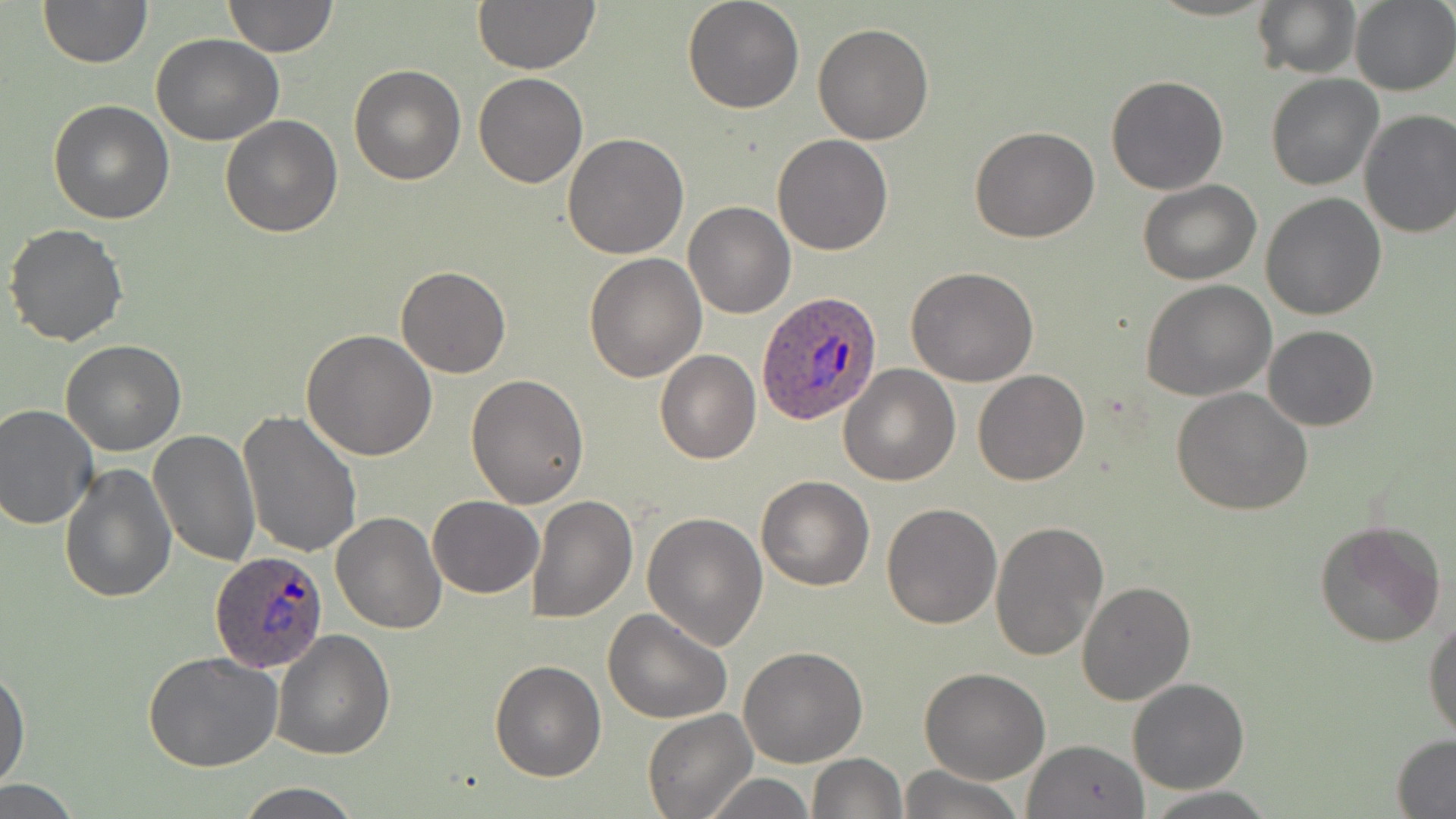 Approximate bounding boxes as (x1, y1, x2, y2) in pixels. Uninfected red blood cell locations: (38, 0, 151, 67), (222, 0, 339, 57), (471, 0, 602, 75), (682, 0, 804, 114), (1251, 0, 1360, 80), (1349, 1, 1456, 94), (812, 22, 936, 145), (151, 33, 283, 146), (349, 63, 466, 185), (473, 73, 588, 188), (1106, 74, 1229, 195), (1265, 74, 1383, 190), (48, 99, 176, 223), (1357, 109, 1456, 239), (221, 116, 343, 238), (970, 127, 1098, 244), (563, 134, 689, 259), (771, 134, 894, 257), (1137, 179, 1262, 285), (1261, 191, 1386, 320), (683, 201, 795, 319), (4, 223, 129, 347), (584, 252, 707, 382), (395, 266, 511, 379), (906, 267, 1039, 387), (1141, 280, 1278, 402), (1263, 325, 1379, 431), (303, 330, 437, 462), (62, 340, 185, 456), (655, 350, 760, 464), (839, 364, 961, 485), (972, 368, 1089, 485), (465, 373, 591, 508), (1171, 386, 1315, 516), (0, 404, 100, 532), (238, 412, 363, 560), (148, 428, 261, 567), (59, 461, 176, 603), (755, 475, 874, 590), (526, 492, 638, 624), (428, 495, 544, 598), (881, 502, 1001, 630), (332, 511, 448, 633), (642, 511, 768, 650), (989, 518, 1109, 661), (1312, 520, 1445, 649), (1076, 579, 1195, 704), (603, 608, 733, 726), (1424, 615, 1456, 742), (274, 629, 395, 759), (738, 646, 868, 767), (142, 652, 284, 772), (489, 660, 606, 782), (0, 665, 30, 790), (920, 667, 1050, 784), (1127, 678, 1250, 794), (644, 708, 755, 818), (1391, 735, 1456, 817), (1022, 739, 1150, 818), (807, 753, 907, 818), (897, 765, 1022, 819), (702, 772, 814, 818), (0, 781, 86, 816), (233, 782, 366, 819), (1144, 788, 1276, 817). Plasmodium ovale-infected red blood cell locations: (759, 292, 882, 426), (211, 550, 330, 672). Slide-level diagnosis: Plasmodium ovale. 1000x magnification. Image is 1456×819 pixels. Thin blood film. Single field of view. Optical microscopy. May-Grünwald-Giemsa stain.